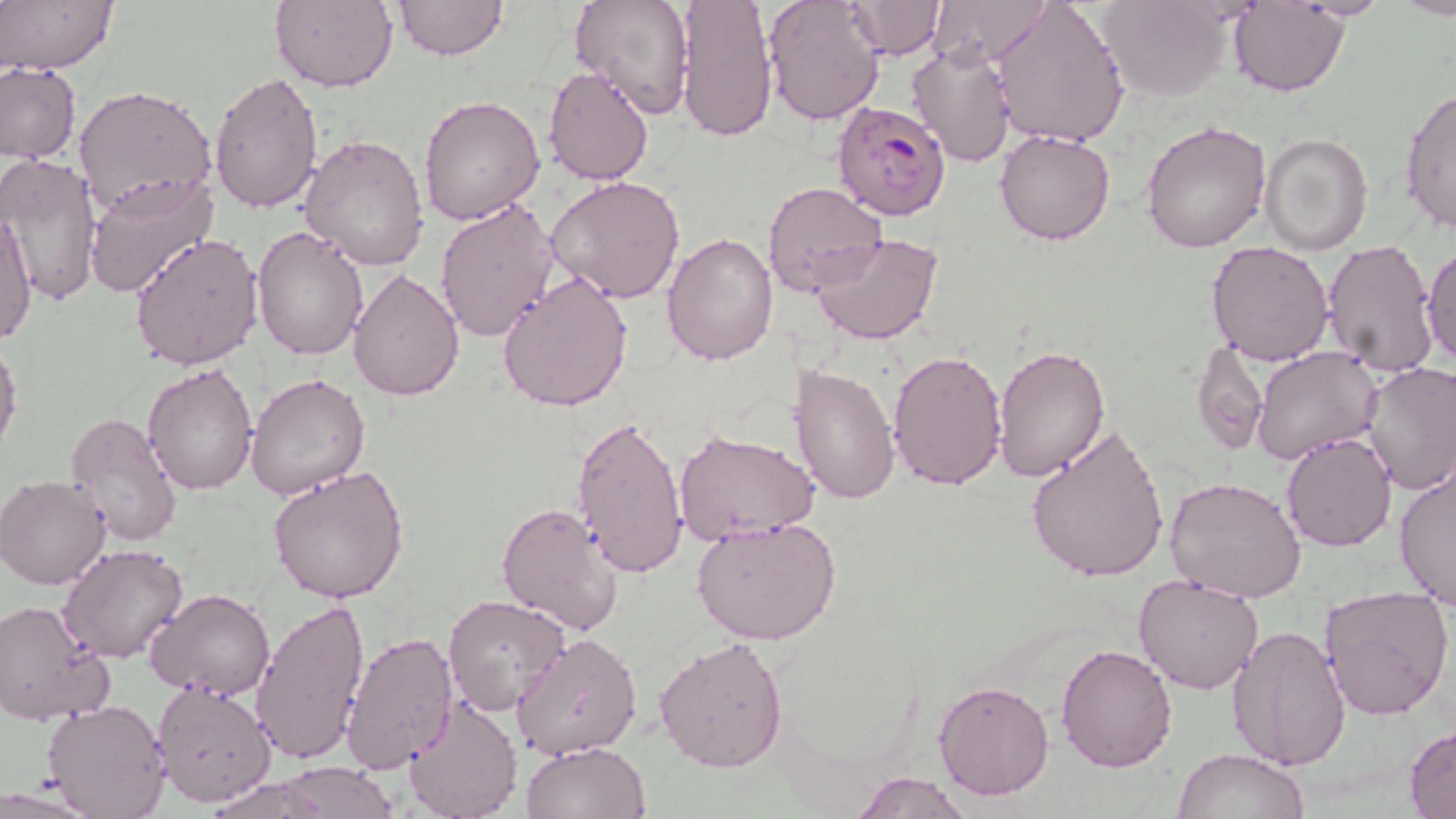 Approximate bounding boxes as [x1, y1, x2, y2] in pixels. Uninfected red blood cell locations: [1, 0, 119, 74], [272, 0, 399, 92], [392, 0, 507, 61], [570, 0, 695, 119], [675, 0, 779, 142], [761, 0, 887, 126], [844, 0, 947, 59], [928, 0, 1055, 68], [990, 0, 1131, 146], [1292, 0, 1392, 20], [1099, 1, 1232, 102], [1229, 2, 1347, 96], [907, 40, 1020, 167], [1, 62, 80, 162], [542, 66, 656, 185], [206, 72, 325, 213], [73, 84, 219, 217], [1399, 88, 1456, 233], [420, 97, 545, 224], [1142, 120, 1271, 251], [993, 128, 1117, 245], [298, 132, 431, 270], [1260, 134, 1374, 255], [0, 152, 104, 308], [83, 174, 218, 298], [545, 175, 687, 304], [762, 181, 888, 297], [435, 201, 559, 344], [1, 208, 37, 344], [252, 223, 370, 360], [662, 231, 779, 365], [811, 232, 946, 347], [130, 233, 262, 370], [1320, 238, 1438, 380], [1205, 240, 1334, 367], [1422, 245, 1455, 367], [348, 267, 465, 400], [497, 271, 636, 413], [0, 334, 23, 461], [1192, 338, 1268, 454], [887, 345, 1009, 491], [1253, 345, 1382, 464], [992, 346, 1110, 481], [789, 361, 901, 506], [141, 362, 259, 496], [1359, 362, 1456, 496], [245, 373, 370, 502], [75, 383, 247, 522], [64, 413, 182, 547], [570, 413, 688, 579], [1026, 426, 1170, 585], [675, 430, 819, 545], [1281, 431, 1398, 551], [1394, 463, 1456, 611], [268, 465, 410, 604], [1, 474, 114, 589], [1165, 476, 1308, 605], [496, 501, 625, 636], [692, 516, 842, 648], [58, 544, 187, 663], [1132, 573, 1264, 695], [1319, 585, 1454, 723], [145, 587, 276, 698], [442, 594, 570, 717], [250, 599, 371, 765], [0, 600, 114, 725], [1230, 604, 1448, 749], [1227, 625, 1350, 771], [342, 631, 458, 774], [509, 632, 640, 758], [653, 637, 787, 773], [1055, 643, 1178, 773], [937, 658, 1174, 785], [151, 680, 277, 808], [933, 680, 1055, 802], [405, 697, 522, 819], [43, 698, 172, 818], [1404, 728, 1455, 816], [520, 739, 651, 819], [1175, 748, 1306, 819], [273, 761, 399, 817], [852, 772, 972, 818], [0, 780, 109, 817]. Plasmodium falciparum-infected red blood cell locations: [831, 101, 952, 220]. Slide-level diagnosis: Plasmodium falciparum. Optical microscopy. 1000x magnification. May-Grünwald-Giemsa-stained preparation. Thin blood smear. One field of a larger specimen. Image is 1456×819 pixels.